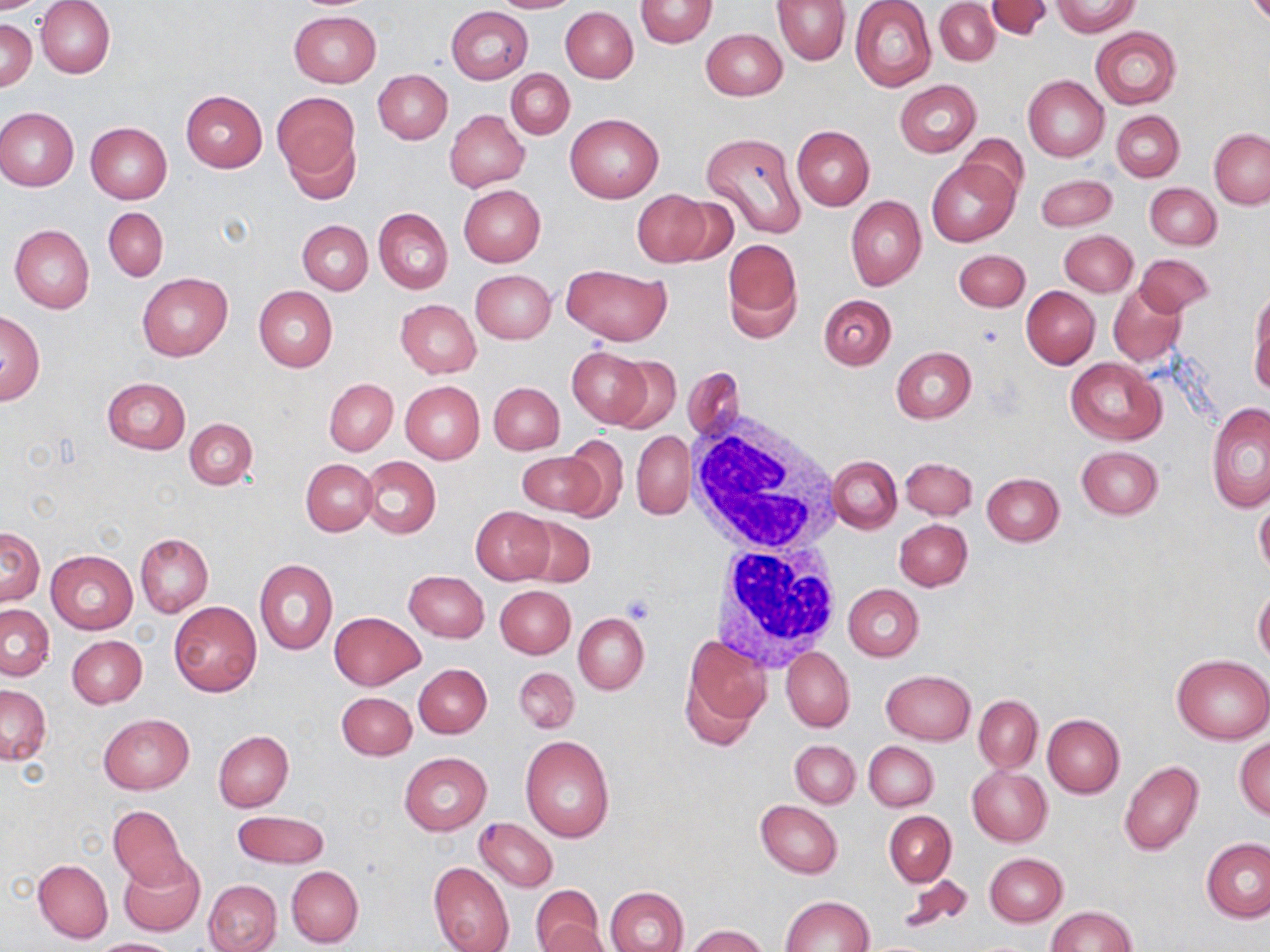
Summary:
  - Coordinate format: approximate bounding boxes as (x1,y1)-(x2,y2) corner pairs in pixels
  - White blood cell locations: (685,407)-(844,555), (710,537)-(845,670)
  - Uninfected red blood cell locations: (0,0)-(53,13), (37,0)-(115,79), (488,0)-(582,13), (636,0)-(717,48), (772,0)-(851,65), (850,0)-(936,91), (935,0)-(1000,66), (1052,0)-(1139,36), (987,1)-(1052,39), (446,6)-(534,85), (561,7)-(638,82), (289,11)-(381,87), (1,20)-(37,90), (1090,26)-(1181,109), (701,27)-(787,100), (506,69)-(574,139), (374,70)-(452,144), (1023,75)-(1109,162), (894,80)-(981,157), (181,90)-(268,172), (273,91)-(360,185), (0,108)-(78,191), (445,110)-(529,191), (1111,110)-(1184,181), (565,114)-(663,202), (86,122)-(171,204), (791,125)-(875,210), (284,128)-(361,206), (1209,129)-(1270,208), (700,130)-(807,240), (957,134)-(1029,200), (927,157)-(1019,247), (1038,174)-(1116,231), (1145,183)-(1221,249), (459,185)-(546,266), (632,189)-(711,266), (845,195)-(926,290), (103,207)-(168,281), (373,207)-(453,295), (298,220)-(373,294), (10,224)-(94,314), (1060,231)-(1138,297), (723,239)-(802,342), (954,250)-(1029,312), (1133,253)-(1215,317), (562,264)-(671,345), (470,269)-(556,344), (137,273)-(232,361), (1107,283)-(1187,366), (253,286)-(338,372), (1021,287)-(1100,368), (1249,287)-(1270,395), (819,295)-(896,369), (395,299)-(481,378), (0,312)-(44,404), (568,347)-(649,425), (891,347)-(976,423), (608,356)-(682,434), (1065,357)-(1166,445), (683,367)-(744,443), (102,377)-(189,454), (324,379)-(397,455), (399,381)-(485,465), (489,381)-(565,454), (1207,401)-(1270,511), (186,418)-(257,490), (632,431)-(693,519), (561,437)-(630,518), (1076,445)-(1164,519), (516,452)-(609,517), (360,456)-(440,539), (828,456)-(901,534), (901,457)-(976,520), (301,459)-(378,535), (982,473)-(1063,546), (1255,497)-(1270,577), (471,506)-(553,583), (516,515)-(596,589), (894,518)-(972,590), (1,526)-(44,605), (135,533)-(212,617), (46,550)-(138,633), (254,559)-(337,655), (404,571)-(489,643), (844,584)-(923,661), (495,585)-(575,659), (1253,588)-(1270,664), (169,601)-(262,697), (1,604)-(54,680), (330,612)-(424,690), (574,614)-(649,695), (67,635)-(146,708), (680,635)-(771,749), (782,647)-(854,731), (1173,654)-(1270,743), (414,663)-(491,738), (513,666)-(579,733), (881,669)-(976,744), (0,685)-(51,764), (337,692)-(416,760), (974,694)-(1042,773), (99,714)-(193,794), (1043,714)-(1124,797), (213,731)-(293,812), (520,735)-(614,842), (1234,736)-(1270,820), (864,740)-(938,811), (790,741)-(860,807), (874,741)-(943,884), (400,751)-(491,834), (1119,760)-(1204,857), (967,765)-(1052,847), (756,800)-(842,878), (106,804)-(193,891), (232,809)-(330,868), (884,811)-(956,885), (474,818)-(558,891), (1201,838)-(1270,923), (984,853)-(1067,927), (116,855)-(205,937), (33,858)-(113,943), (428,861)-(514,952), (287,865)-(364,947), (896,873)-(974,936), (203,879)-(281,952), (531,884)-(604,952), (606,887)-(689,952), (781,895)-(874,950), (1045,906)-(1136,951), (539,922)-(612,952), (685,924)-(769,952), (92,938)-(182,951)
  - Platelet locations: (975,324)-(1005,349), (623,594)-(655,623)
  - Slide-level diagnosis: negative for blood parasites
  - Field of view: one of a larger specimen
  - Modality: optical microscopy
  - Image size: 1270×952 pixels
  - Preparation: thin blood smear
  - Magnification: 1000x
  - Stain: May-Grünwald-Giemsa